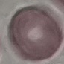
Result: no malaria parasites detected. Automatically extracted cell patch, resized to 64 × 64 pixels. Giemsa-stained preparation. Thin blood film. Photographed with a smartphone camera at the microscope eyepiece.